Assess this cell for malaria.
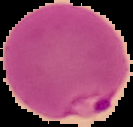

Parasitized.

Summary:
  - Image size: 133×127 pixels
  - Preparation: thin blood smear
  - Image type: segmented cell region with the area outside set to black